Assess the morphology of the red blood cells.
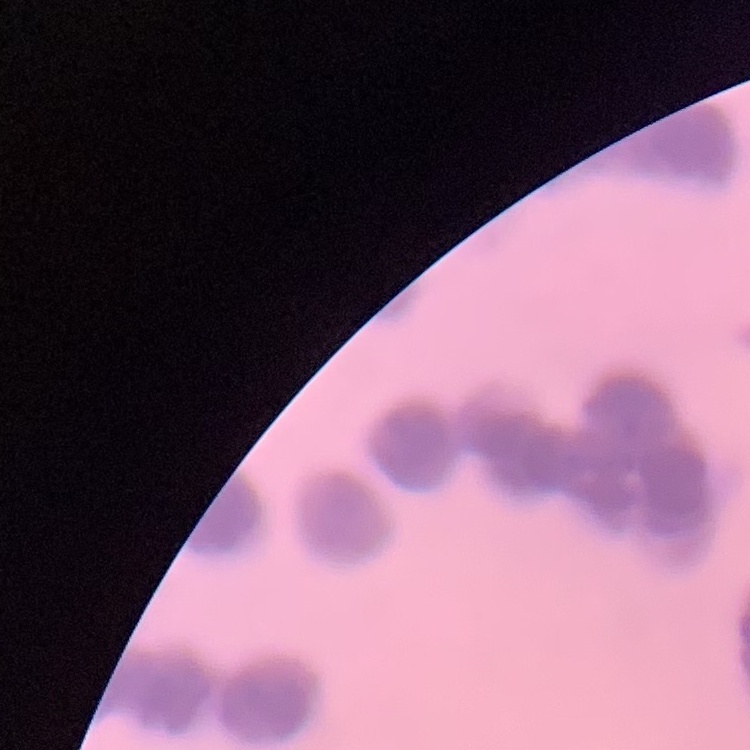
Rouleaux formation.

image type = one tile cut from a larger photomicrograph
stain = Field's or Giemsa
preparation = thin peripheral smear